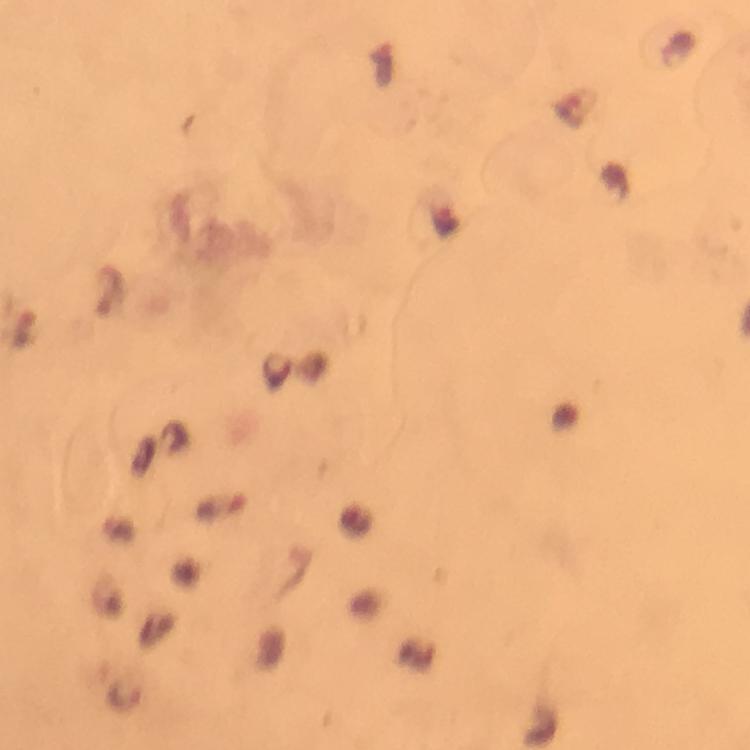

capture: smartphone photograph through a microscope
immersion_oil: used
plasmodium_parasite_locations: 'approximate centers as [x, y] in pixels: [577, 106], [221, 505], [127, 696]'
stain: Giemsa
preparation: thick blood smear
image_size: 750×750 pixels
magnification: 100x
cropped_from: a single field of view
context: from a diagnostic examination for malaria